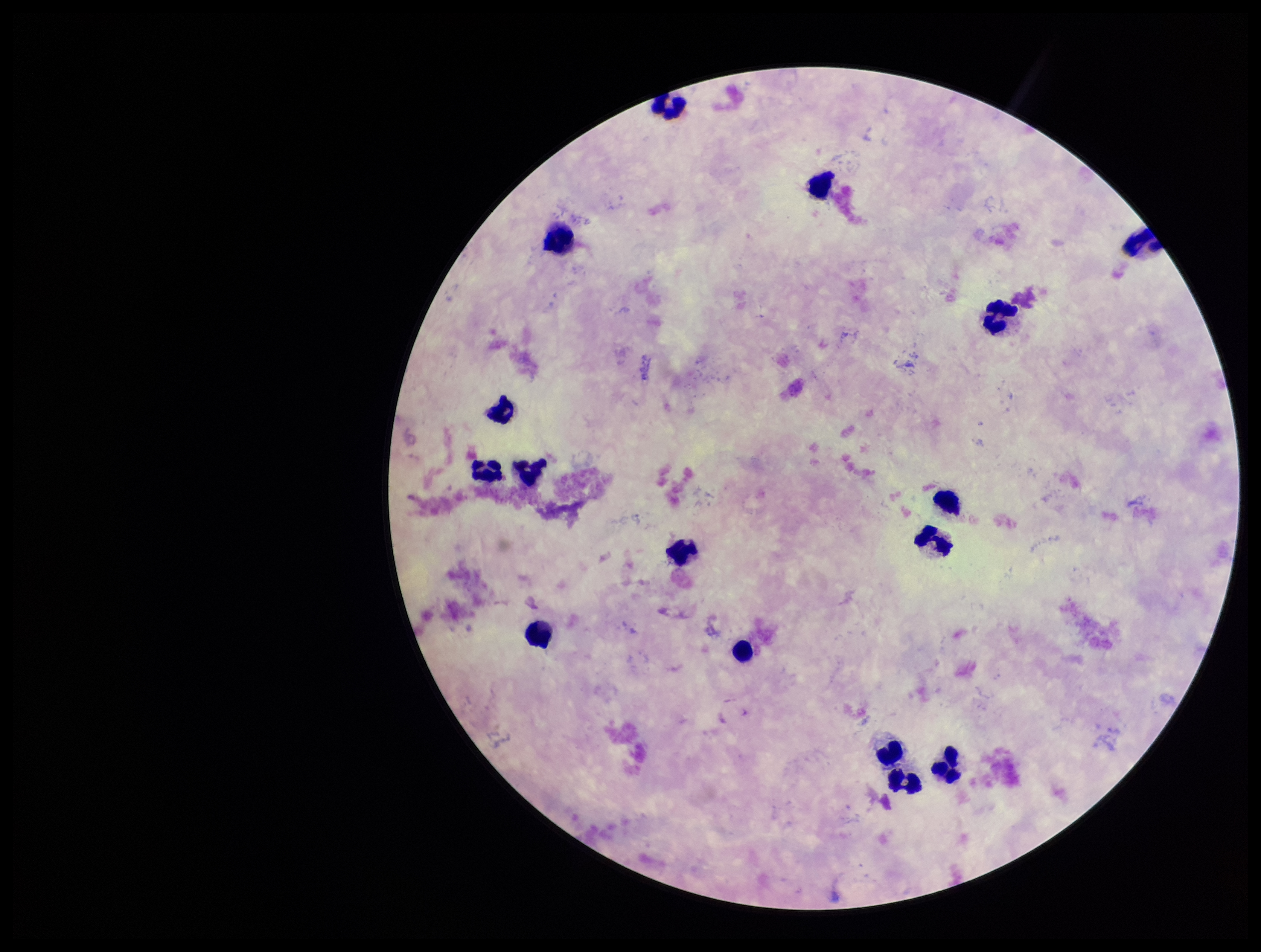
Summary:
  - Stain: Giemsa
  - Parasite count: 0
  - Preparation: thick
  - Plasmodium parasites: none detected
  - Patient malaria status: negative
  - Image size: 1261×952 pixels
  - Capture: smartphone photograph through the microscope eyepiece
  - Field of view: one from this slide
  - Leukocyte count: 16